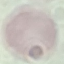

Summary:
  - Result: no malaria parasites detected
  - Stain: Giemsa
  - Image type: cell patch, automatically extracted from a larger field of view and resized to 64 × 64 pixels
  - Capture: smartphone camera at the microscope eyepiece
  - Preparation: thin blood smear